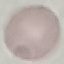 Result: no malaria parasites seen. Giemsa-stained preparation. Thin blood film. Cell patch, automatically extracted from a larger field of view and resized to 64 × 64 pixels. Acquired by smartphone through the microscope eyepiece.